Mark where platelets are.
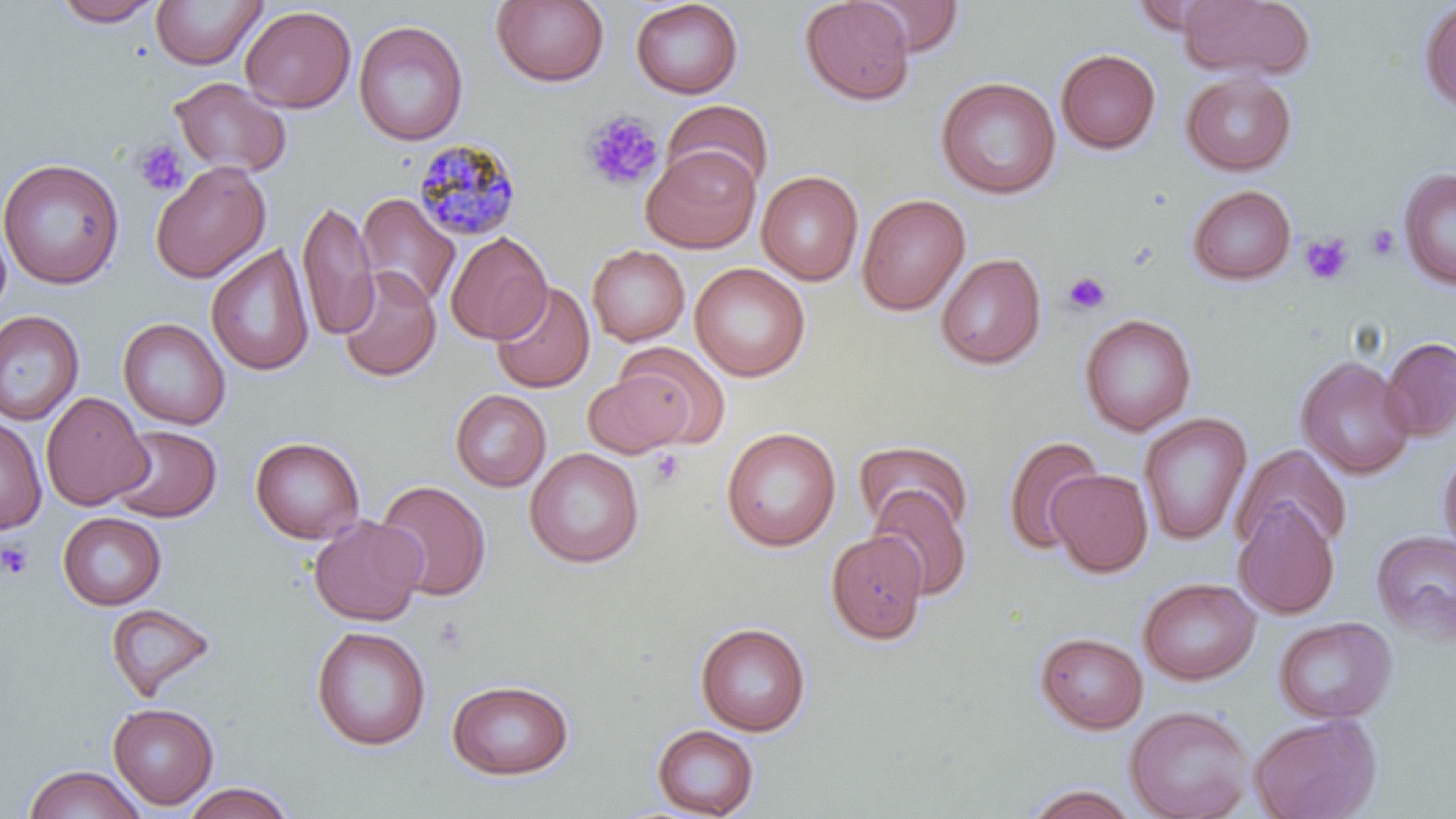
Approximate bounding boxes as named x1/y1/x2/y2 corners in pixels.
Platelets: (x1=580, y1=110, x2=662, y2=191), (x1=134, y1=140, x2=189, y2=196), (x1=1366, y1=225, x2=1401, y2=260), (x1=1301, y1=233, x2=1354, y2=286), (x1=1063, y1=271, x2=1110, y2=315), (x1=647, y1=449, x2=685, y2=491), (x1=0, y1=539, x2=34, y2=580), (x1=433, y1=617, x2=470, y2=655).

slide-level diagnosis = Plasmodium malariae
preparation = thin blood smear
uninfected red blood cell locations = approximate bounding boxes as named x1/y1/x2/y2 corners in pixels: (x1=52, y1=0, x2=163, y2=27), (x1=151, y1=0, x2=266, y2=70), (x1=630, y1=0, x2=744, y2=99), (x1=799, y1=0, x2=916, y2=106), (x1=859, y1=0, x2=965, y2=57), (x1=1179, y1=0, x2=1313, y2=80), (x1=491, y1=1, x2=610, y2=87), (x1=1418, y1=3, x2=1456, y2=114), (x1=240, y1=5, x2=356, y2=113), (x1=353, y1=20, x2=468, y2=146), (x1=1056, y1=48, x2=1161, y2=155), (x1=1181, y1=71, x2=1296, y2=176), (x1=936, y1=76, x2=1061, y2=200), (x1=169, y1=77, x2=291, y2=177), (x1=660, y1=99, x2=774, y2=195), (x1=641, y1=148, x2=760, y2=253), (x1=0, y1=158, x2=124, y2=289), (x1=150, y1=161, x2=271, y2=283), (x1=1397, y1=168, x2=1456, y2=290), (x1=757, y1=170, x2=864, y2=285), (x1=1187, y1=185, x2=1297, y2=286), (x1=356, y1=193, x2=460, y2=309), (x1=857, y1=194, x2=971, y2=315), (x1=298, y1=200, x2=377, y2=342), (x1=445, y1=231, x2=552, y2=345), (x1=206, y1=244, x2=315, y2=378), (x1=587, y1=244, x2=690, y2=346), (x1=935, y1=253, x2=1047, y2=370), (x1=690, y1=263, x2=810, y2=382), (x1=337, y1=264, x2=441, y2=383), (x1=491, y1=282, x2=595, y2=393), (x1=0, y1=309, x2=85, y2=426), (x1=1078, y1=313, x2=1197, y2=436), (x1=118, y1=318, x2=231, y2=430), (x1=1381, y1=337, x2=1456, y2=441), (x1=608, y1=345, x2=729, y2=449), (x1=1296, y1=355, x2=1416, y2=480), (x1=582, y1=371, x2=694, y2=457), (x1=450, y1=389, x2=551, y2=492), (x1=41, y1=391, x2=152, y2=511), (x1=1138, y1=412, x2=1252, y2=546), (x1=0, y1=416, x2=46, y2=535), (x1=109, y1=425, x2=222, y2=522), (x1=721, y1=426, x2=841, y2=552), (x1=1002, y1=435, x2=1104, y2=556), (x1=249, y1=436, x2=366, y2=544), (x1=853, y1=440, x2=974, y2=539), (x1=1232, y1=444, x2=1353, y2=557), (x1=1437, y1=446, x2=1456, y2=558), (x1=525, y1=447, x2=645, y2=568), (x1=1047, y1=469, x2=1153, y2=577), (x1=375, y1=479, x2=492, y2=601), (x1=867, y1=487, x2=973, y2=601), (x1=1234, y1=503, x2=1340, y2=618), (x1=57, y1=512, x2=167, y2=610), (x1=308, y1=515, x2=426, y2=626), (x1=1371, y1=530, x2=1456, y2=644), (x1=825, y1=531, x2=929, y2=646), (x1=1137, y1=577, x2=1260, y2=685), (x1=105, y1=602, x2=217, y2=703), (x1=1273, y1=616, x2=1396, y2=724), (x1=695, y1=623, x2=811, y2=736), (x1=311, y1=625, x2=431, y2=751), (x1=1035, y1=632, x2=1148, y2=734), (x1=447, y1=679, x2=574, y2=780), (x1=108, y1=703, x2=218, y2=809), (x1=1125, y1=705, x2=1254, y2=819), (x1=1248, y1=713, x2=1383, y2=819), (x1=651, y1=725, x2=759, y2=818), (x1=23, y1=764, x2=147, y2=819), (x1=181, y1=782, x2=296, y2=819), (x1=1020, y1=784, x2=1143, y2=818)
stain = May-Grünwald-Giemsa
magnification = 1000x
modality = light microscopy
field of view = one of a larger specimen
image size = 1456×819 pixels
Plasmodium malariae-infected red blood cell locations = approximate bounding boxes as named x1/y1/x2/y2 corners in pixels: (x1=412, y1=137, x2=522, y2=241)